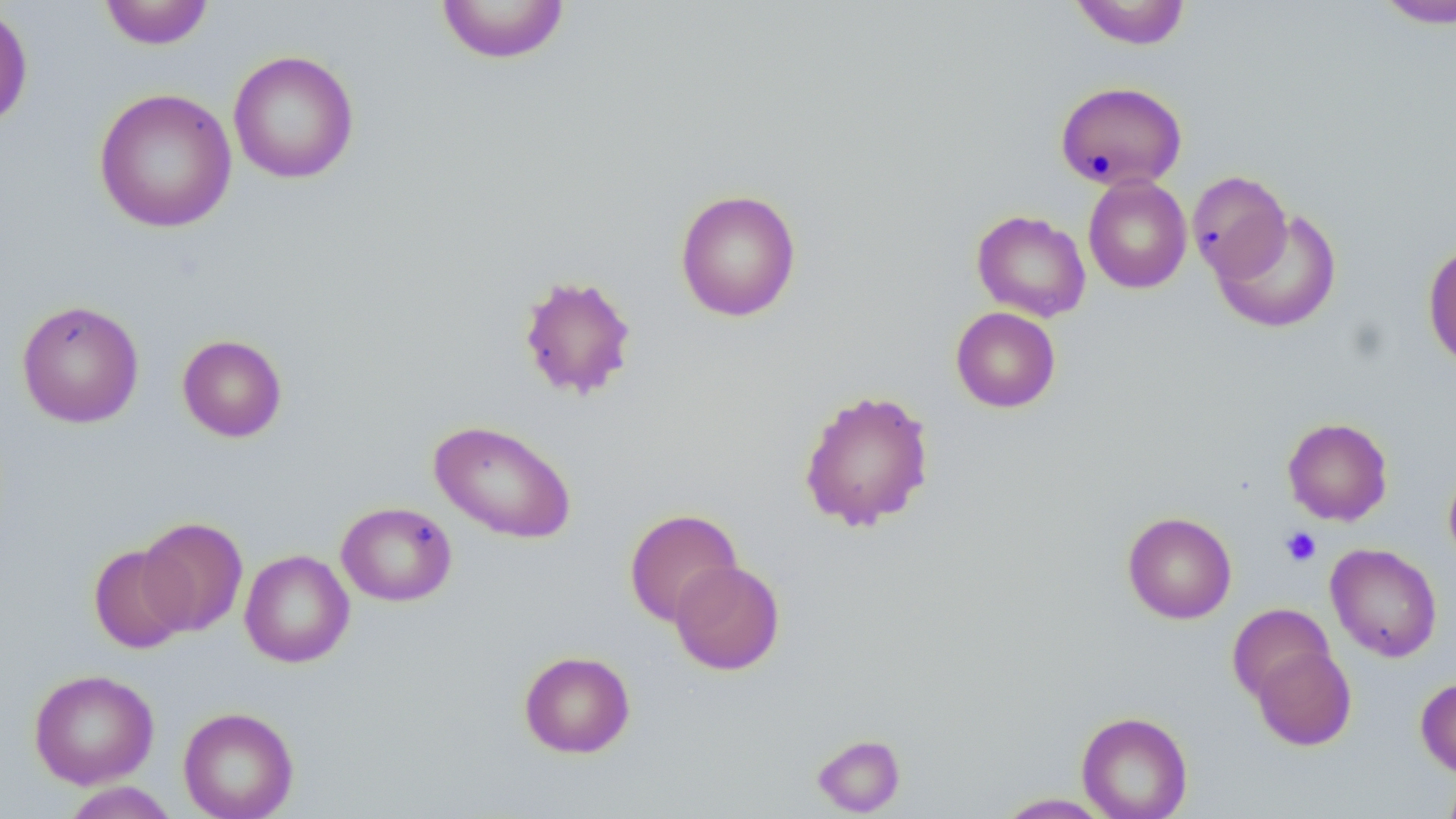
Summary:
  - Coordinate format: approximate bounding boxes as (x1,y1)-(x2,y2) corner pairs in pixels
  - Uninfected red blood cell locations (subset): (98,0)-(215,50), (435,0)-(571,64), (1068,0)-(1192,50), (1374,0)-(1456,28), (0,4)-(33,130), (228,49)-(359,184), (1055,81)-(1188,191), (93,87)-(237,233), (1187,170)-(1292,282), (1083,175)-(1192,294), (675,189)-(801,322), (1213,207)-(1342,333), (971,210)-(1091,322), (1423,242)-(1456,368), (518,273)-(638,402), (17,299)-(144,428), (950,307)-(1061,413), (177,334)-(288,442), (797,388)-(935,533), (1282,417)-(1393,526), (429,419)-(577,544), (1443,462)-(1456,570), (336,502)-(457,606), (624,508)-(742,626), (1122,512)-(1237,624), (137,516)-(247,636), (88,543)-(191,654), (1326,543)-(1442,662), (239,549)-(355,668), (669,559)-(785,675), (1227,603)-(1334,703), (1251,645)-(1356,751), (519,650)-(635,758), (29,668)-(159,789), (1415,677)-(1456,778), (178,706)-(299,819), (1077,711)-(1193,819), (1440,769)-(1456,819), (60,781)-(181,819), (993,792)-(1117,818)
  - Platelet locations (subset): (1280,526)-(1322,567)
  - Slide-level diagnosis: no evidence of blood parasites
  - Image size: 1456×819 pixels
  - Stain: May-Grünwald-Giemsa
  - Preparation: thin blood smear
  - Field of view: single
  - Magnification: 1000x
  - Modality: light microscopy